Give the position of every leukocyte visible.
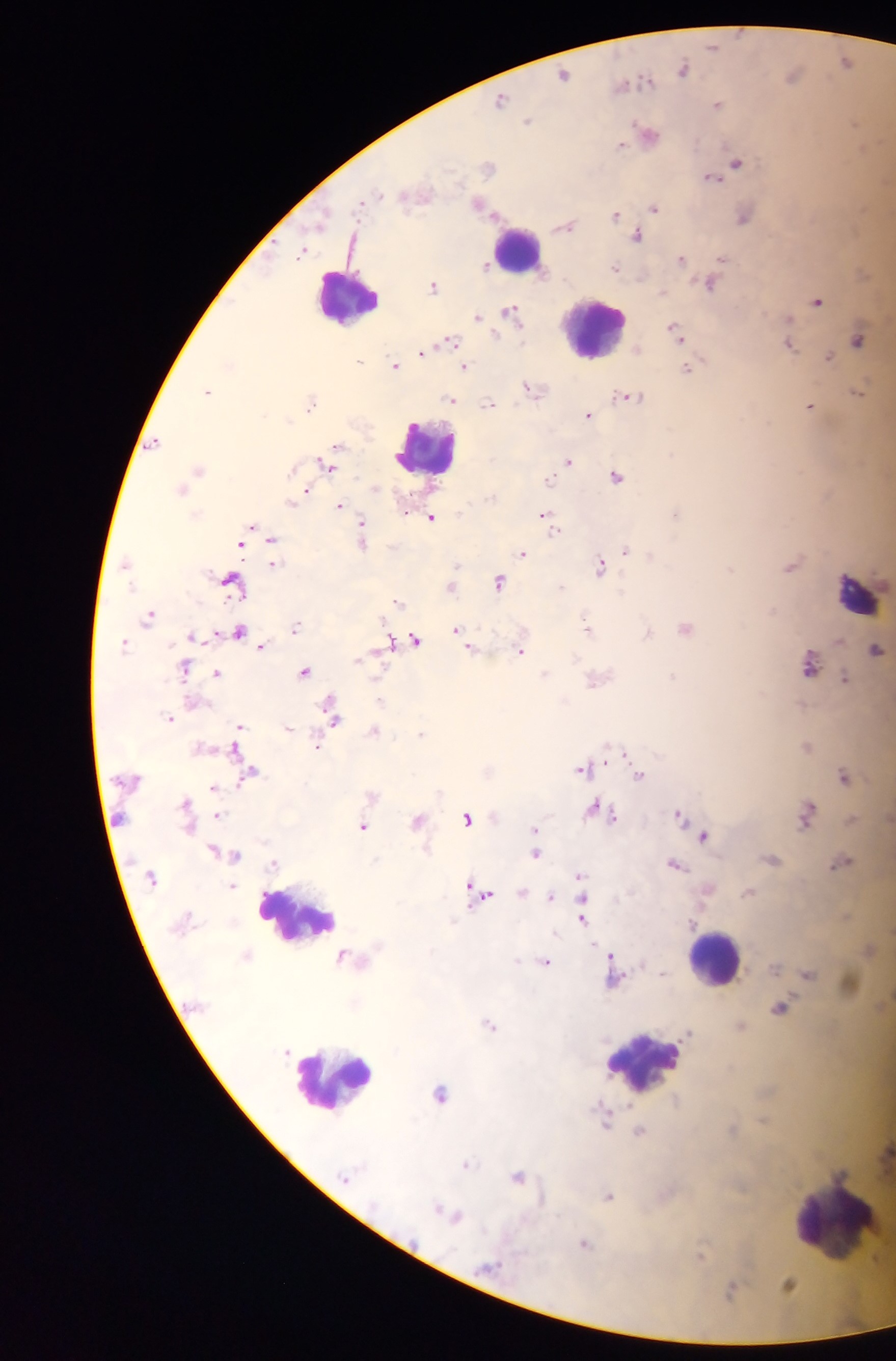

Approximate centers as (x, y) in pixels.
Leukocytes: (517, 248), (347, 295), (592, 328), (426, 447), (856, 593), (295, 917), (713, 958), (643, 1067), (334, 1079), (846, 1222).

Summary:
  - Malaria parasite locations: (712, 45), (846, 61), (682, 69), (564, 74), (790, 75), (641, 81), (623, 85), (500, 99), (717, 104), (527, 121), (855, 123), (647, 133), (619, 144), (736, 163), (488, 167), (711, 177), (479, 204), (653, 207), (614, 215), (743, 217), (564, 226), (637, 236), (301, 252), (680, 259), (720, 259), (484, 266), (615, 268), (709, 285), (432, 286), (816, 301), (510, 312), (477, 317), (674, 332), (450, 340), (856, 340), (787, 345), (422, 351), (828, 357), (359, 361), (394, 364), (228, 365), (464, 366), (686, 369), (529, 387), (207, 391), (857, 391), (626, 397), (449, 400), (311, 401), (487, 404), (808, 407), (587, 416), (153, 443), (332, 451), (568, 461), (326, 463), (198, 469), (616, 477), (548, 479), (180, 490), (302, 495), (296, 499), (340, 506), (675, 513), (431, 518), (548, 521), (250, 528), (552, 529), (362, 536), (271, 538), (626, 551), (523, 553), (273, 563), (599, 566), (789, 566), (229, 581), (497, 582), (450, 585), (398, 602), (149, 617), (586, 625), (295, 627), (684, 628), (457, 631), (238, 632), (646, 634), (194, 637), (414, 640), (465, 641), (123, 644), (387, 644), (262, 646), (469, 647), (520, 650), (875, 650), (809, 665), (184, 669), (304, 671), (217, 672), (544, 674), (671, 676), (843, 678), (596, 680), (380, 701), (333, 716), (169, 717), (238, 727), (288, 728), (373, 732), (421, 733), (806, 746), (317, 747), (616, 752), (583, 768), (250, 773), (638, 775), (842, 776), (214, 788), (185, 804), (597, 810), (805, 813), (217, 815), (609, 815), (678, 815), (467, 819), (416, 821), (362, 826), (534, 829), (702, 837), (534, 854), (234, 855), (770, 859), (840, 862), (674, 864), (578, 877), (746, 892), (521, 893), (480, 894), (549, 897), (581, 919), (869, 949), (610, 955), (544, 962), (661, 972), (612, 978), (780, 1008), (489, 1024), (686, 1033), (439, 1093), (604, 1120), (639, 1130), (465, 1164), (516, 1176), (608, 1196), (438, 1208), (453, 1215), (583, 1244), (788, 1283), (730, 1290)
  - Image size: 896×1361 pixels
  - Capture: mobile-phone photograph through a microscope
  - Country: Ghana
  - Field of view: single
  - Preparation: thick blood smear